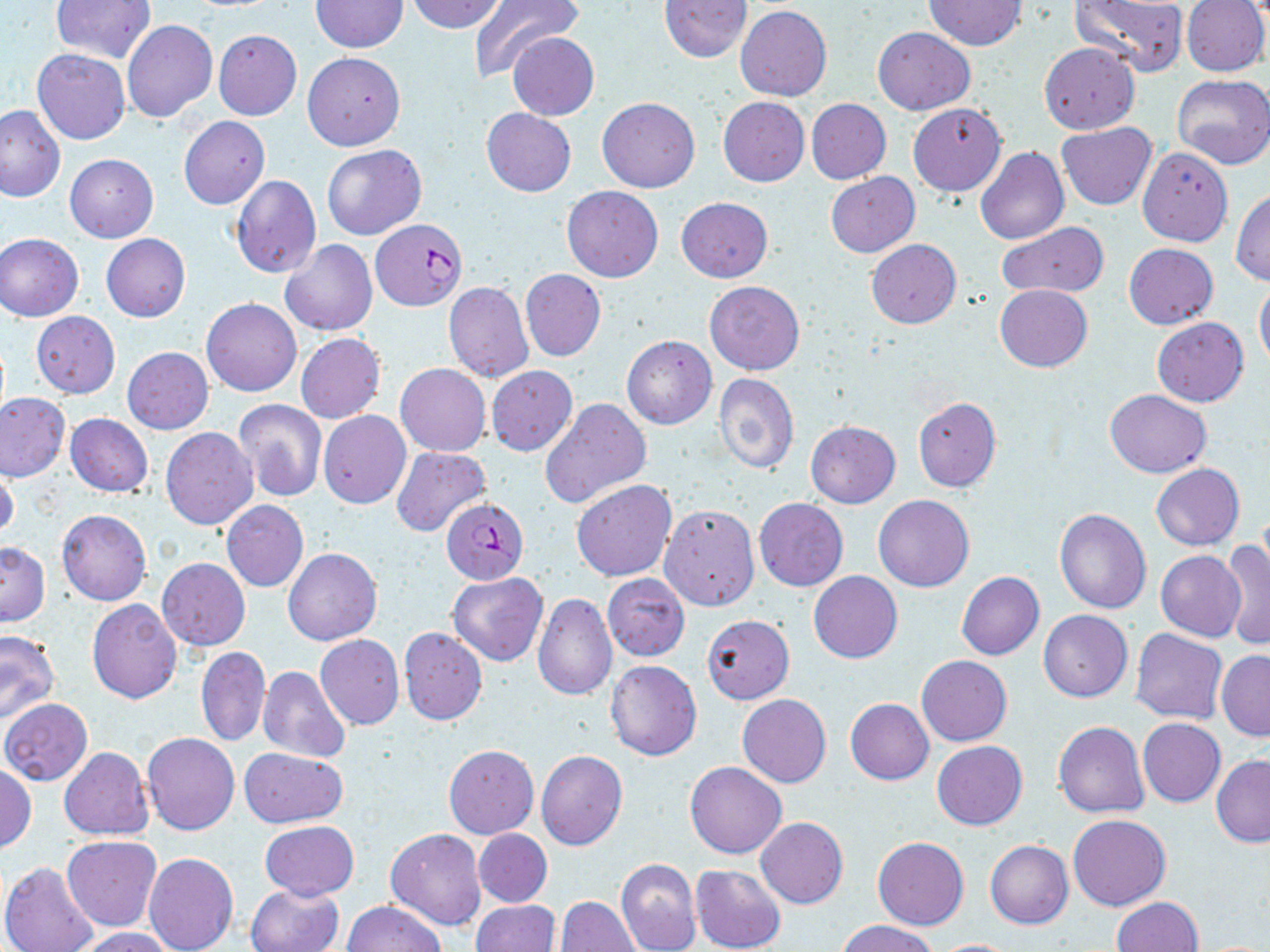

slide-level diagnosis = Plasmodium falciparum
magnification = 1000x
preparation = thin blood film
uninfected red blood cell locations = approximate bounding boxes as [x1, y1, x2, y2] in pixels: [50, 0, 155, 65], [407, 0, 505, 33], [469, 0, 582, 81], [1070, 0, 1186, 76], [1182, 0, 1269, 76], [309, 1, 409, 51], [659, 1, 752, 62], [923, 1, 1026, 49], [736, 6, 831, 100], [122, 20, 218, 122], [872, 27, 975, 115], [213, 30, 302, 120], [507, 33, 598, 120], [1039, 42, 1140, 132], [32, 49, 129, 144], [302, 52, 405, 151], [1170, 75, 1270, 170], [718, 96, 809, 186], [597, 97, 700, 193], [806, 98, 891, 184], [908, 103, 1005, 196], [0, 105, 64, 202], [481, 108, 576, 197], [178, 115, 270, 209], [1057, 123, 1156, 210], [322, 145, 427, 241], [975, 146, 1069, 245], [1137, 147, 1233, 246], [65, 153, 158, 243], [825, 172, 921, 258], [231, 175, 320, 278], [561, 186, 664, 282], [1231, 189, 1270, 285], [685, 195, 781, 360], [677, 197, 773, 282], [996, 223, 1110, 299], [1, 234, 84, 321], [101, 234, 191, 322], [866, 239, 961, 328], [279, 240, 377, 337], [1124, 243, 1218, 328], [520, 268, 606, 361], [705, 280, 804, 374], [1254, 280, 1270, 374], [444, 282, 534, 382], [995, 284, 1091, 372], [201, 298, 301, 397], [31, 311, 120, 398], [1152, 317, 1250, 406], [295, 333, 385, 424], [621, 335, 717, 429], [123, 346, 213, 434], [394, 363, 490, 455], [486, 366, 578, 456], [714, 373, 800, 475], [1105, 390, 1211, 478], [0, 394, 70, 480], [540, 398, 651, 509], [913, 398, 1001, 491], [234, 399, 327, 501], [319, 410, 411, 509], [65, 413, 154, 498], [806, 421, 900, 507], [161, 427, 258, 530], [392, 446, 492, 537], [1150, 463, 1244, 551], [0, 466, 20, 543], [571, 479, 677, 581], [874, 494, 974, 592], [754, 499, 848, 591], [222, 500, 308, 591], [659, 504, 759, 611], [1054, 508, 1151, 614], [57, 509, 151, 606], [1221, 539, 1270, 650], [0, 542, 49, 625], [283, 548, 382, 645], [1155, 551, 1245, 641], [158, 558, 250, 650], [809, 570, 902, 663], [448, 571, 548, 666], [956, 571, 1045, 660], [602, 573, 690, 662], [533, 593, 618, 701], [87, 600, 181, 704], [1039, 610, 1132, 702], [702, 615, 795, 704], [399, 627, 488, 726], [1131, 629, 1227, 724], [0, 630, 59, 725], [315, 635, 404, 730], [196, 646, 270, 747], [1217, 652, 1270, 740], [917, 655, 1011, 746], [605, 660, 701, 761], [258, 665, 351, 764], [737, 694, 832, 788], [845, 697, 933, 785], [1, 698, 93, 786], [1138, 718, 1225, 806], [1053, 721, 1149, 818], [142, 732, 240, 835], [932, 740, 1027, 830], [444, 745, 538, 838], [58, 746, 153, 839], [238, 747, 347, 828], [536, 749, 627, 850], [1211, 755, 1270, 847], [685, 762, 786, 859], [0, 764, 36, 852], [1067, 812, 1171, 911], [756, 816, 848, 909], [260, 821, 359, 899], [387, 826, 487, 932], [474, 829, 552, 907], [62, 836, 161, 931], [872, 837, 969, 930], [985, 840, 1073, 928], [145, 852, 239, 952], [615, 857, 701, 952], [0, 861, 98, 952], [691, 864, 786, 952], [246, 884, 343, 952], [556, 896, 641, 952], [1110, 897, 1203, 952], [341, 901, 444, 951], [472, 902, 559, 952], [837, 920, 939, 952], [72, 927, 177, 951], [927, 938, 1028, 951]
field of view = one of a larger specimen
stain = May-Grünwald-Giemsa
Plasmodium falciparum-infected red blood cell locations = approximate bounding boxes as [x1, y1, x2, y2] in pixels: [370, 219, 466, 310], [441, 498, 529, 584]
image size = 1270×952 pixels
modality = optical microscopy